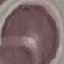
Malaria status: uninfected. Automatically extracted cell patch, resized to 64 × 64 pixels. Thin smear of blood. Giemsa stain. Acquired by smartphone through the microscope eyepiece.